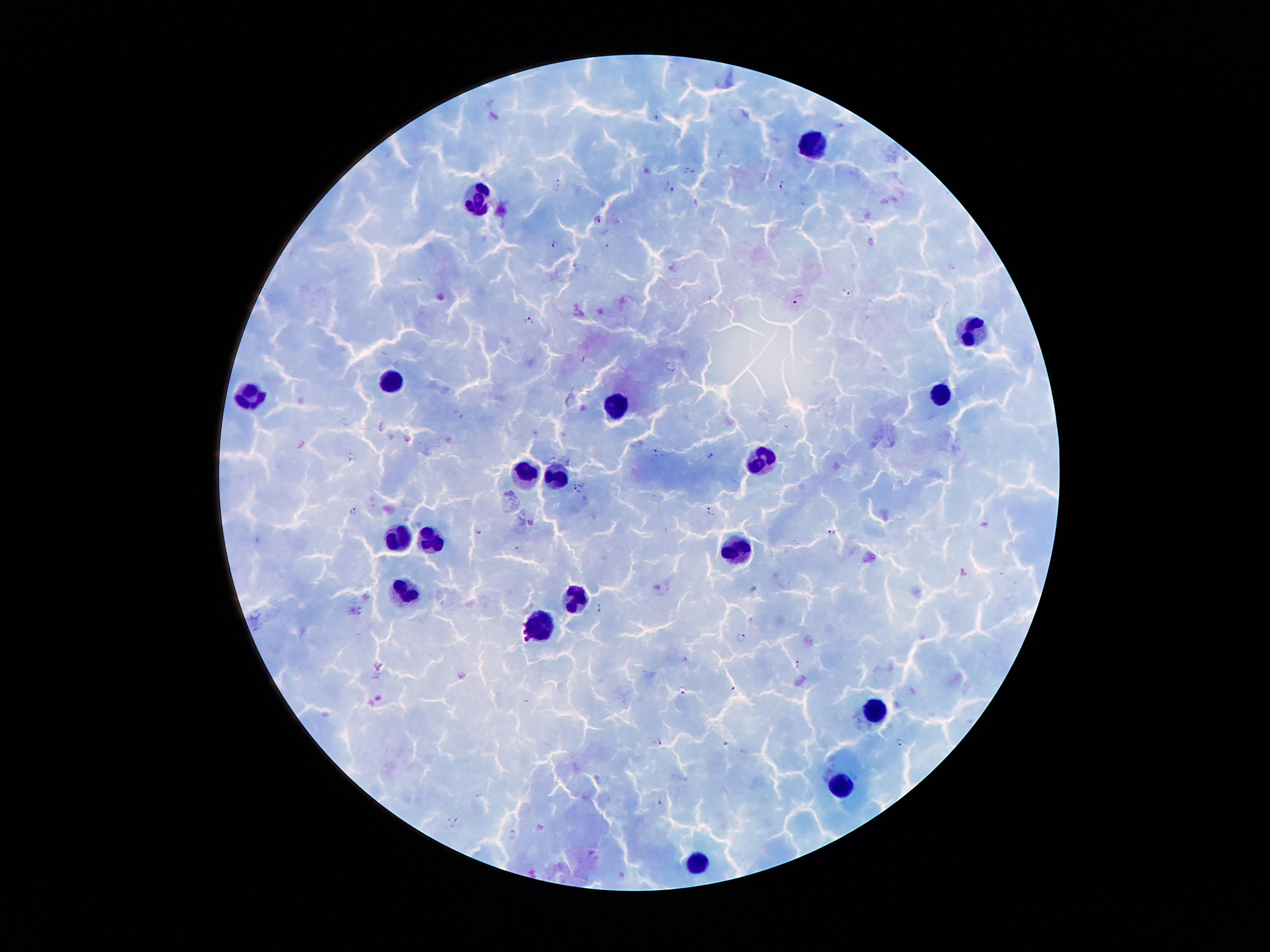

Approximate object centers, in pixels from the top-left corner.
Summary:
  - Leukocyte locations: (x=811, y=145), (x=481, y=200), (x=972, y=331), (x=392, y=381), (x=941, y=395), (x=248, y=397), (x=613, y=404), (x=764, y=461), (x=523, y=473), (x=559, y=475), (x=391, y=536), (x=429, y=541), (x=734, y=554), (x=409, y=593), (x=574, y=599), (x=542, y=626), (x=875, y=712), (x=841, y=787), (x=697, y=860)
  - Plasmodium parasite locations: (x=658, y=117), (x=841, y=125), (x=721, y=154), (x=690, y=170), (x=557, y=182), (x=780, y=184), (x=672, y=191), (x=554, y=244), (x=607, y=247), (x=846, y=292), (x=797, y=299), (x=529, y=320), (x=667, y=363), (x=536, y=432), (x=406, y=438), (x=655, y=452), (x=711, y=455), (x=352, y=456), (x=577, y=488), (x=354, y=511), (x=711, y=512), (x=478, y=532), (x=832, y=532), (x=518, y=548), (x=598, y=607), (x=360, y=608), (x=352, y=610), (x=742, y=636), (x=797, y=661), (x=379, y=666), (x=462, y=675), (x=733, y=688), (x=683, y=690), (x=661, y=740), (x=899, y=742), (x=660, y=800), (x=455, y=821)
  - Magnification: 100x
  - Capture: smartphone through the microscope eyepiece
  - Patient malaria status: infected with Plasmodium falciparum
  - Image size: 1270×952 pixels
  - Preparation: thick peripheral-blood smear
  - Stain: Giemsa
  - Field of view: one from this slide